Locate every Plasmodium falciparum-infected red blood cell.
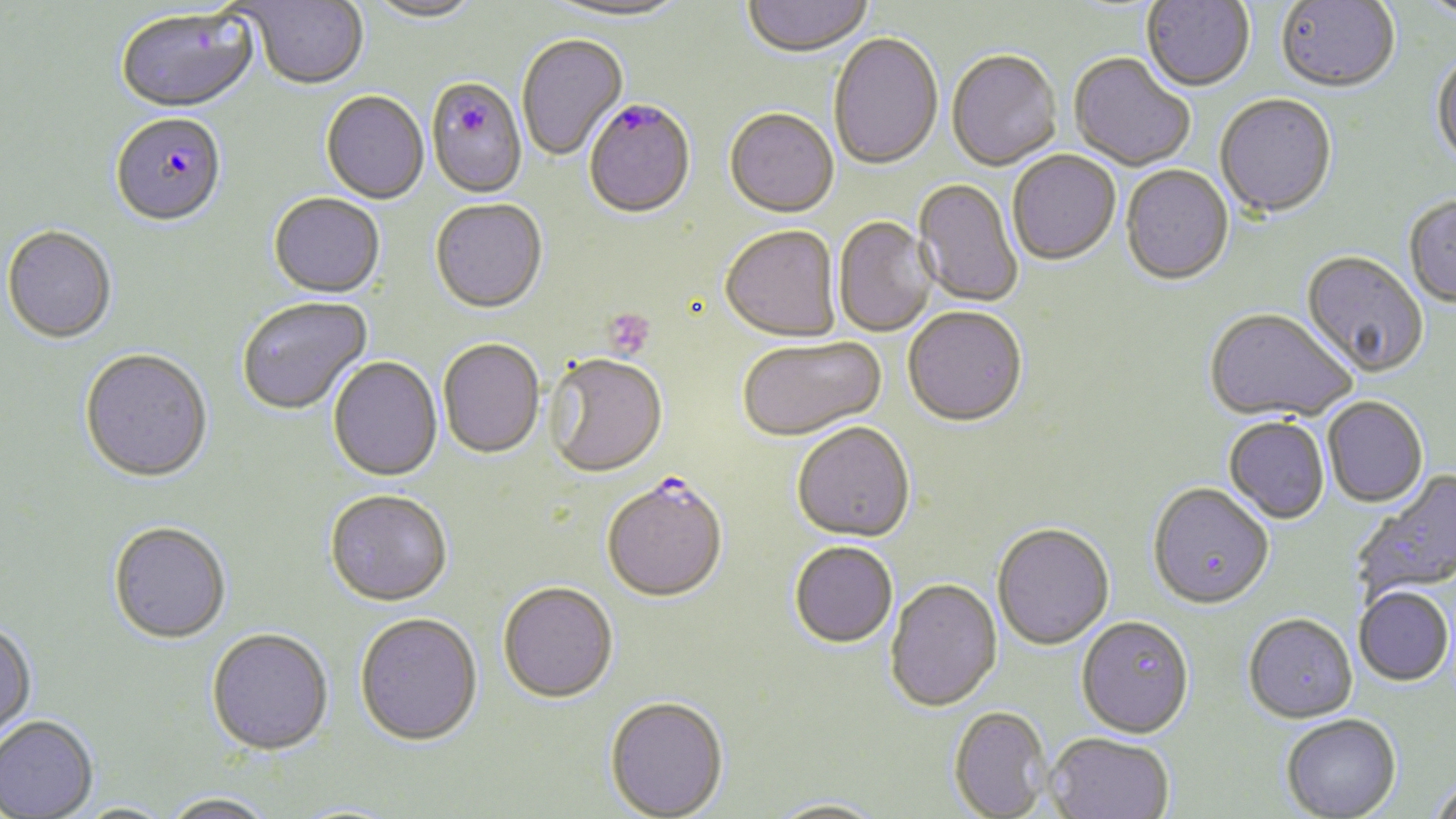
Approximate bounding boxes as (x1,y1)-(x2,y2) corner pairs in pixels.
Plasmodium falciparum-infected red blood cells: (426,80)-(527,200), (584,101)-(696,221), (111,116)-(227,230), (601,480)-(728,606).

slide-level diagnosis = Plasmodium falciparum
stain = May-Grünwald-Giemsa
image size = 1456×819 pixels
modality = light microscopy
platelet locations = approximate bounding boxes as (x1,y1)-(x2,y2) corner pairs in pixels: (603,309)-(655,361)
uninfected red blood cell locations = approximate bounding boxes as (x1,y1)-(x2,y2) corner pairs in pixels: (364,0)-(484,25), (545,0)-(689,25), (741,0)-(874,60), (1142,0)-(1255,93), (1276,0)-(1400,95), (1418,1)-(1456,24), (247,2)-(368,91), (115,9)-(260,116), (517,35)-(628,163), (828,35)-(944,173), (946,52)-(1062,173), (1068,55)-(1194,172), (1431,55)-(1456,171), (321,92)-(429,205), (1215,95)-(1337,222), (724,110)-(839,220), (1007,152)-(1121,267), (1120,166)-(1234,288), (913,179)-(1023,309), (268,194)-(386,300), (1404,197)-(1456,309), (430,201)-(547,316), (833,217)-(938,338), (2,228)-(117,346), (720,228)-(841,344), (1300,253)-(1428,380), (237,298)-(373,417), (903,309)-(1028,431), (1203,310)-(1355,424), (737,338)-(886,444), (439,341)-(545,461), (79,351)-(214,485), (328,357)-(443,484), (545,357)-(669,481), (1322,399)-(1428,509), (1223,419)-(1330,526), (791,425)-(915,546), (1352,469)-(1456,601), (1147,485)-(1274,613), (325,492)-(453,609), (109,524)-(231,646), (991,525)-(1115,653), (789,544)-(898,650), (885,580)-(1003,715), (497,585)-(618,706), (1354,588)-(1454,688), (355,616)-(483,750), (1243,617)-(1357,726), (1076,618)-(1194,741), (0,623)-(38,748), (206,631)-(333,758), (604,699)-(729,819), (948,707)-(1053,818), (1281,716)-(1403,819), (0,717)-(99,818), (1046,734)-(1174,819), (1426,780)-(1456,819), (160,794)-(279,819), (762,798)-(891,818)
field of view = one of a larger specimen
preparation = thin blood film
magnification = 1000x